Identify the parasite.
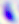

Toxoplasma gondii.

Micrograph. Captured at 400x magnification.